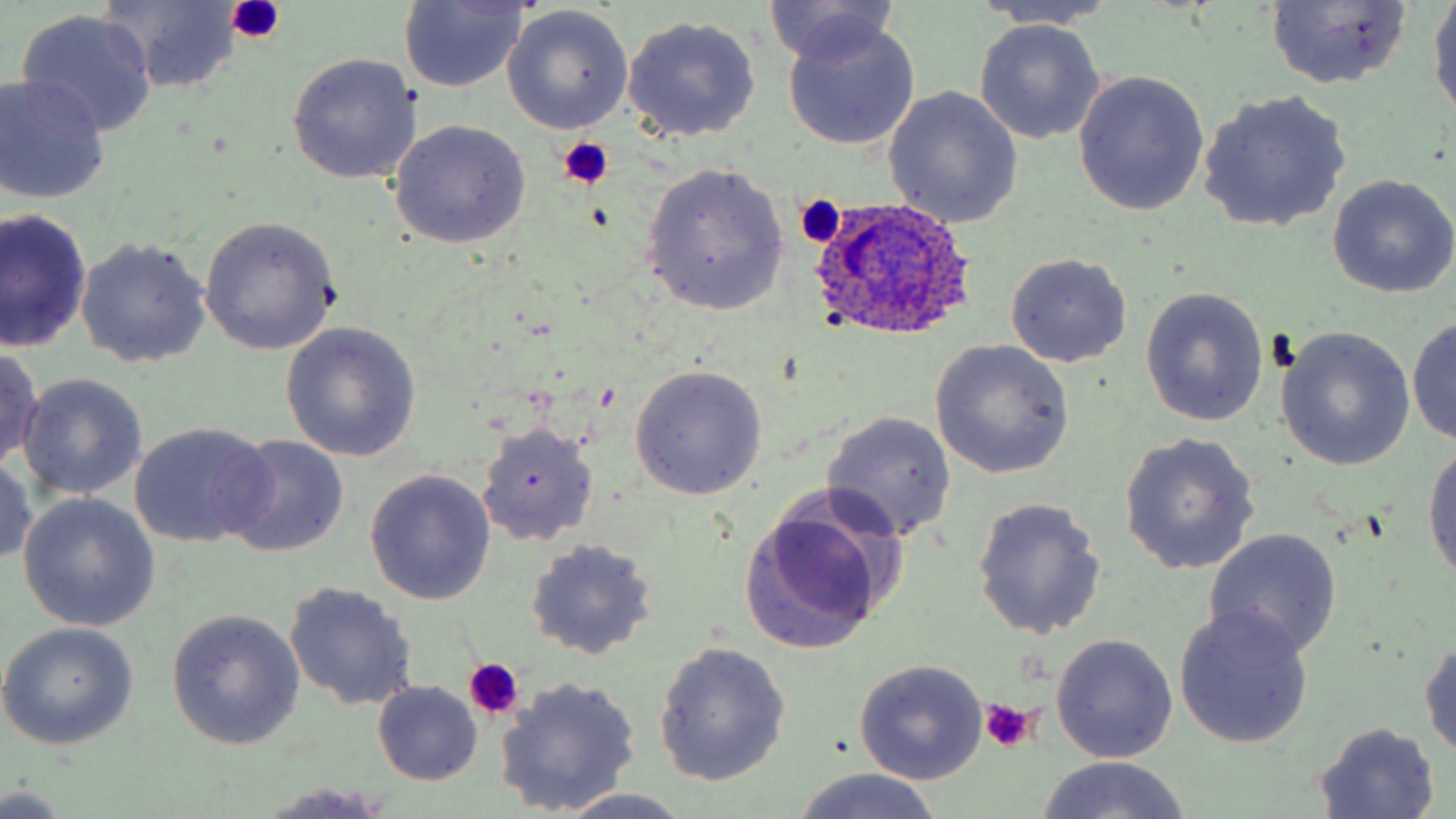
slide_level_diagnosis: Plasmodium ovale
platelet_locations: 'approximate bounding boxes as (x1,y1)-(x2,y2) corner pairs in pixels: (226,0)-(286,42), (558,137)-(615,190), (795,194)-(847,248), (463,659)-(526,721), (977,700)-(1042,756)'
stain: May-Grünwald-Giemsa
plasmodium_ovale_infected_red_blood_cell_locations: 'approximate bounding boxes as (x1,y1)-(x2,y2) corner pairs in pixels: (808,197)-(977,345)'
image_size: 1456×819 pixels
field_of_view: one of a larger specimen
preparation: thin blood film
magnification: 1000x
modality: light microscopy
uninfected_red_blood_cell_locations: 'approximate bounding boxes as (x1,y1)-(x2,y2) corner pairs in pixels: (1429,0)-(1456,121), (398,1)-(528,93), (765,1)-(904,70), (98,2)-(247,90), (971,2)-(1122,31), (1265,2)-(1413,90), (504,7)-(635,134), (16,10)-(157,136), (621,14)-(762,143), (781,16)-(921,152), (975,19)-(1106,144), (285,53)-(422,185), (1072,72)-(1208,216), (0,73)-(112,204), (882,87)-(1024,229), (1198,89)-(1353,234), (388,119)-(531,249), (641,160)-(791,315), (1326,174)-(1456,299), (1,209)-(92,354), (198,217)-(339,354), (76,237)-(211,367), (1005,253)-(1133,368), (1141,287)-(1269,427), (1408,316)-(1456,445), (280,323)-(421,462), (1274,327)-(1416,472), (929,340)-(1074,479), (0,347)-(45,471), (629,365)-(768,500), (18,374)-(146,501), (821,412)-(957,542), (130,421)-(276,548), (476,422)-(598,547), (1119,433)-(1261,575), (220,436)-(350,557), (1422,438)-(1456,594), (0,454)-(38,569), (365,469)-(497,604), (19,493)-(158,632), (971,497)-(1107,639), (739,501)-(895,654), (1204,527)-(1343,659), (526,538)-(658,660), (284,582)-(419,711), (1173,604)-(1315,750), (167,611)-(304,749), (0,623)-(140,751), (1051,634)-(1179,763), (1419,636)-(1456,764), (655,641)-(791,785), (853,661)-(988,785), (494,675)-(642,816), (373,682)-(482,785), (1311,723)-(1443,816), (1035,756)-(1194,819), (789,767)-(947,819), (0,784)-(72,816), (261,784)-(397,817), (548,790)-(698,819)'